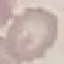

Malaria status: uninfected. Giemsa stain. Automatically extracted cell patch, resized to 64 × 64 pixels. Acquired by smartphone through the microscope eyepiece. Thin blood film.